Assess the morphology of the erythrocytes.
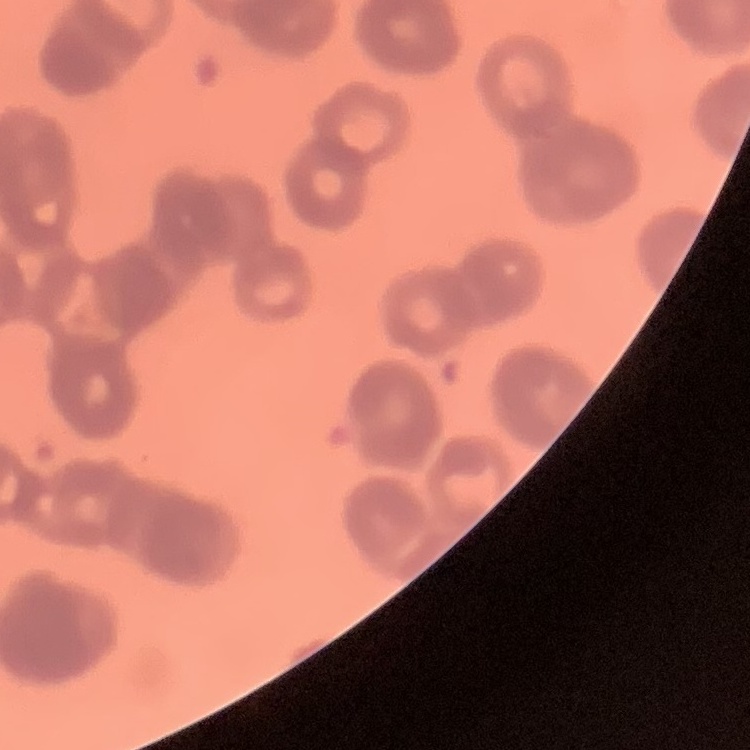

Rouleaux formation.

Field's or Giemsa stain. One tile cut from a larger photomicrograph. Thin blood smear.